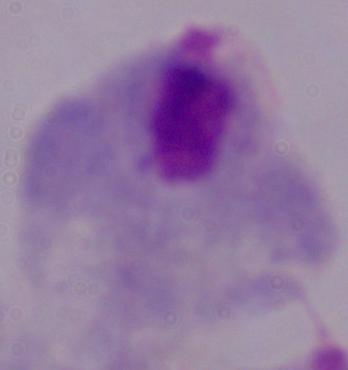
identification = trichomonad
magnification = 1000x
modality = micrograph